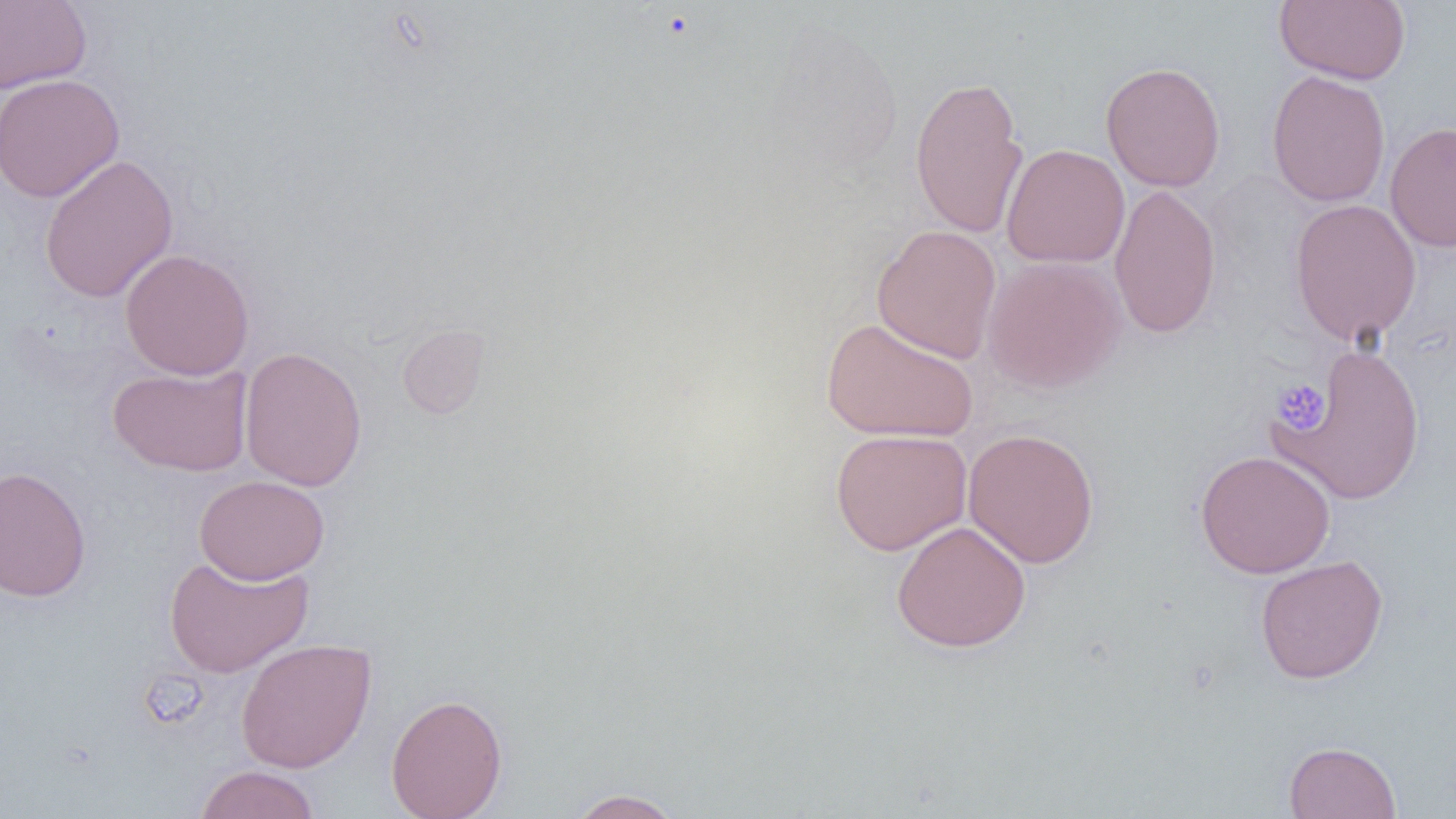
Approximate bounding boxes as (x1, y1, x2, y2) in pixels. Uninfected red blood cell locations: (1274, 0, 1411, 85), (0, 1, 92, 93), (1100, 61, 1226, 192), (1266, 70, 1391, 208), (0, 73, 124, 203), (909, 75, 1029, 239), (1385, 122, 1456, 252), (1002, 143, 1130, 268), (38, 153, 178, 303), (1108, 183, 1222, 339), (1289, 198, 1423, 346), (872, 224, 1002, 363), (119, 249, 255, 380), (982, 255, 1127, 395), (821, 317, 979, 442), (397, 324, 490, 420), (1277, 344, 1427, 505), (239, 346, 368, 491), (107, 364, 253, 476), (962, 427, 1100, 569), (830, 428, 972, 556), (1195, 450, 1335, 578), (0, 465, 92, 602), (194, 475, 330, 584), (891, 520, 1031, 653), (163, 553, 314, 678), (1254, 554, 1389, 684), (235, 638, 376, 773), (386, 693, 507, 819), (1283, 741, 1401, 819), (195, 765, 320, 819), (567, 789, 684, 818). Platelet locations: (1272, 378, 1331, 434). Slide-level diagnosis: negative for blood parasites. Captured at 1000x magnification. One field of a larger specimen. Image is 1456×819 pixels. Optical microscopy. Thin blood smear.